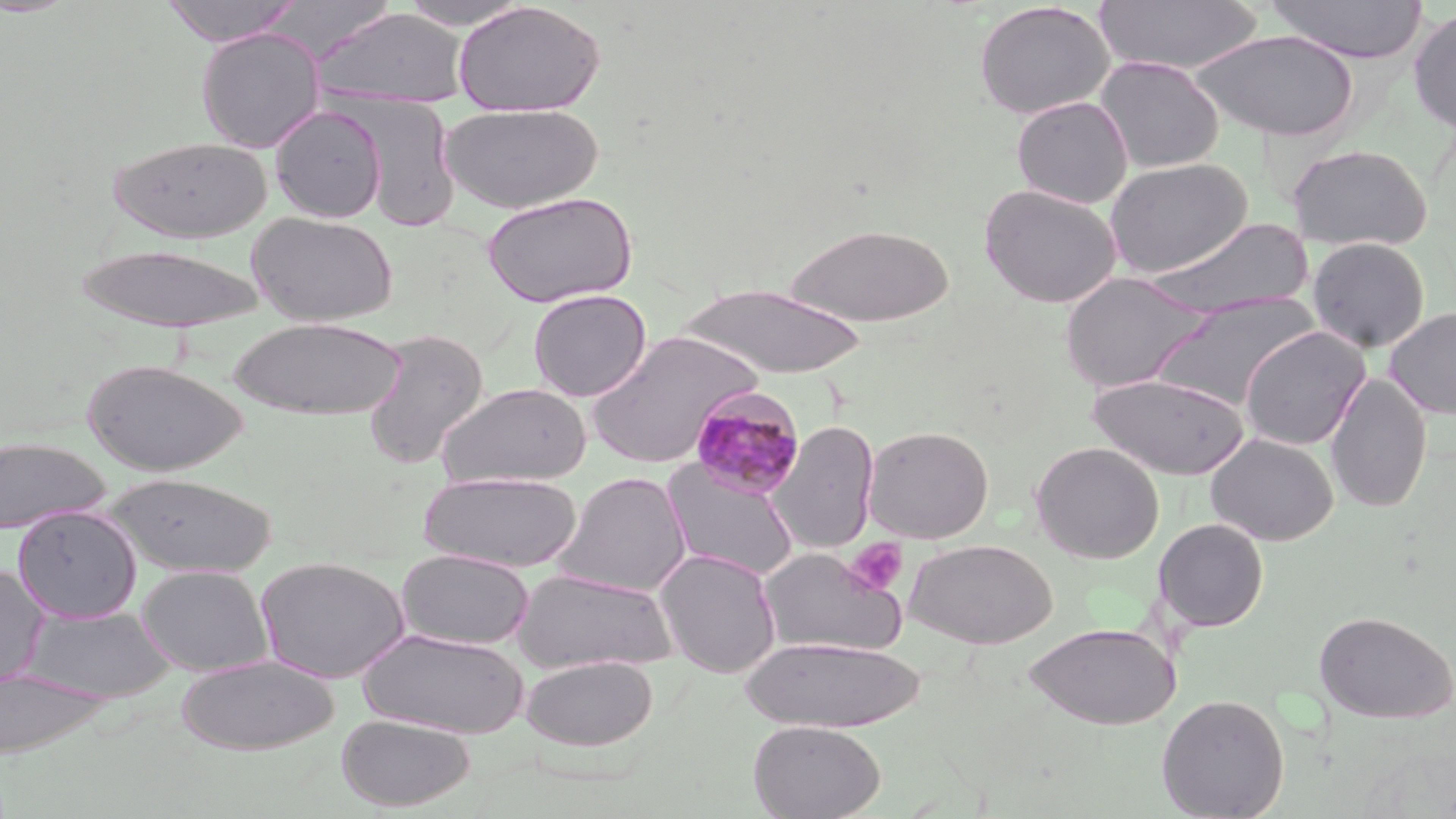
slide-level diagnosis = Plasmodium malariae
magnification = 1000x
platelet locations = approximate bounding boxes as named x1/y1/x2/y2 corners in pixels: (x1=845, y1=538, x2=908, y2=594)
Plasmodium malariae-infected red blood cell locations = approximate bounding boxes as named x1/y1/x2/y2 corners in pixels: (x1=687, y1=385, x2=806, y2=499)
uninfected red blood cell locations = approximate bounding boxes as named x1/y1/x2/y2 corners in pixels: (x1=159, y1=0, x2=304, y2=46), (x1=1265, y1=0, x2=1429, y2=64), (x1=397, y1=1, x2=531, y2=30), (x1=452, y1=1, x2=606, y2=117), (x1=1093, y1=1, x2=1263, y2=75), (x1=973, y1=2, x2=1115, y2=119), (x1=311, y1=7, x2=469, y2=109), (x1=1408, y1=7, x2=1456, y2=135), (x1=195, y1=27, x2=326, y2=153), (x1=1191, y1=29, x2=1359, y2=142), (x1=1093, y1=56, x2=1225, y2=173), (x1=345, y1=96, x2=461, y2=232), (x1=1011, y1=96, x2=1133, y2=209), (x1=441, y1=102, x2=604, y2=214), (x1=270, y1=105, x2=387, y2=223), (x1=107, y1=135, x2=272, y2=243), (x1=1287, y1=143, x2=1433, y2=252), (x1=1104, y1=158, x2=1253, y2=278), (x1=979, y1=184, x2=1123, y2=308), (x1=482, y1=190, x2=638, y2=308), (x1=247, y1=211, x2=398, y2=326), (x1=1144, y1=217, x2=1312, y2=320), (x1=783, y1=223, x2=954, y2=327), (x1=1307, y1=237, x2=1430, y2=354), (x1=75, y1=244, x2=267, y2=331), (x1=1059, y1=271, x2=1212, y2=393), (x1=677, y1=283, x2=868, y2=381), (x1=527, y1=289, x2=652, y2=401), (x1=1152, y1=292, x2=1321, y2=413), (x1=1385, y1=307, x2=1456, y2=420), (x1=227, y1=316, x2=407, y2=420), (x1=1239, y1=326, x2=1370, y2=450), (x1=361, y1=328, x2=489, y2=471), (x1=585, y1=331, x2=761, y2=468), (x1=83, y1=359, x2=248, y2=475), (x1=1087, y1=371, x2=1249, y2=480), (x1=1325, y1=372, x2=1431, y2=515), (x1=437, y1=382, x2=592, y2=488), (x1=770, y1=420, x2=880, y2=554), (x1=863, y1=426, x2=993, y2=543), (x1=1205, y1=433, x2=1339, y2=546), (x1=0, y1=436, x2=110, y2=533), (x1=1030, y1=441, x2=1164, y2=564), (x1=662, y1=460, x2=800, y2=581), (x1=417, y1=471, x2=583, y2=573), (x1=554, y1=471, x2=691, y2=596), (x1=104, y1=472, x2=277, y2=578), (x1=13, y1=506, x2=141, y2=622), (x1=1153, y1=518, x2=1269, y2=632), (x1=904, y1=539, x2=1058, y2=649), (x1=759, y1=547, x2=908, y2=657), (x1=396, y1=548, x2=534, y2=650), (x1=655, y1=549, x2=782, y2=677), (x1=255, y1=555, x2=409, y2=683), (x1=137, y1=564, x2=273, y2=676), (x1=0, y1=566, x2=49, y2=688), (x1=511, y1=568, x2=679, y2=674), (x1=21, y1=606, x2=178, y2=703), (x1=1313, y1=610, x2=1456, y2=724), (x1=1025, y1=622, x2=1181, y2=729), (x1=359, y1=627, x2=530, y2=739), (x1=742, y1=636, x2=923, y2=733), (x1=175, y1=655, x2=339, y2=754), (x1=522, y1=655, x2=658, y2=751), (x1=0, y1=667, x2=112, y2=760), (x1=1155, y1=694, x2=1290, y2=819), (x1=336, y1=713, x2=475, y2=811), (x1=748, y1=719, x2=885, y2=819)
stain = May-Grünwald-Giemsa
image size = 1456×819 pixels
preparation = thin blood smear
modality = light microscopy
field of view = single